Classify the preparation.
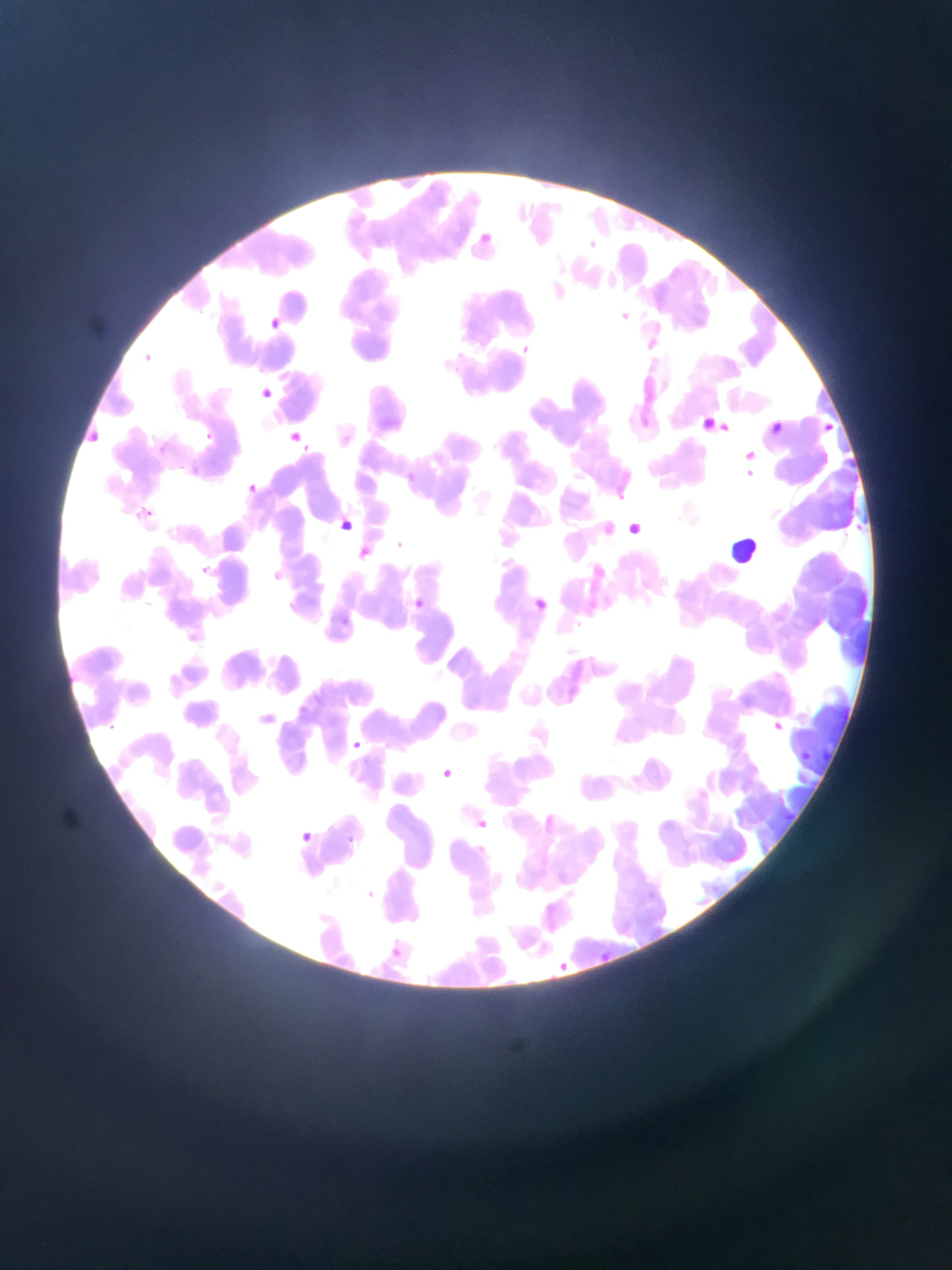
Thin blood smear.

Approximate bounding boxes as left top right bottom in pixels. Malaria parasite locations: 515 341 534 355; 140 350 157 369; 820 424 835 436; 203 426 216 445; 286 428 304 446; 283 430 308 452; 747 466 768 490; 244 480 260 496; 137 504 157 523; 329 513 358 538; 853 519 869 533; 394 531 413 554; 192 561 216 581; 264 565 286 584; 526 593 553 619; 412 595 432 619; 337 613 356 629; 774 717 789 733; 99 720 118 736; 344 737 365 756; 797 748 811 763; 434 765 458 786; 472 815 492 834; 292 828 317 850; 344 832 353 847; 471 840 491 858; 358 885 379 905; 382 940 408 962; 602 947 621 969; 560 958 581 977. Sample from Ghana. One field of view. Mobile-phone photograph taken through the microscope. Image is 952×1270 pixels.